Identify the parasite.
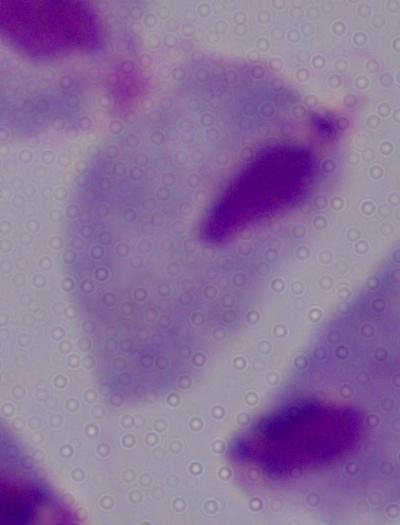
This is a trichomonad.

magnification = 1000x
modality = micrograph